Point out each leukocyte.
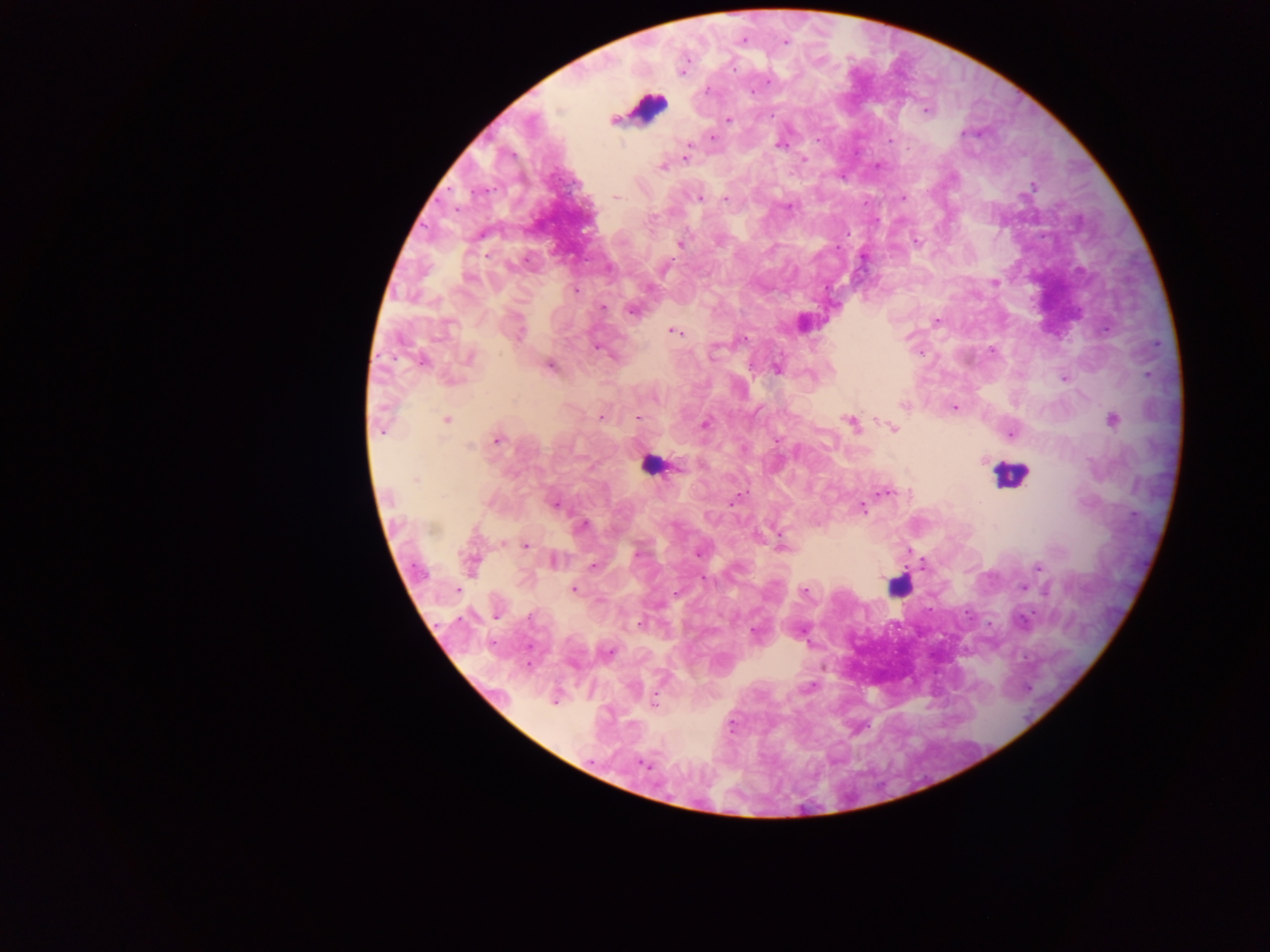
Approximate centers as [x, y] in pixels.
Leukocytes: [648, 108], [650, 465], [1008, 473], [899, 586].

Summary:
  - Malaria parasite locations: [744, 40], [786, 42], [733, 68], [683, 73], [768, 81], [707, 91], [750, 92], [926, 110], [613, 120], [729, 120], [965, 133], [712, 137], [817, 139], [890, 140], [688, 145], [780, 145], [686, 158], [803, 160], [662, 167], [1033, 185], [616, 197], [700, 198], [903, 198], [725, 199], [789, 206], [917, 241], [680, 244], [667, 266], [469, 278], [995, 282], [575, 291], [603, 308], [632, 311], [936, 322], [675, 332], [743, 339], [992, 350], [469, 358], [423, 362], [549, 366], [777, 368], [1064, 378], [655, 399], [903, 405], [954, 407], [601, 418], [637, 419], [1113, 419], [446, 420], [851, 422], [705, 425], [893, 428], [1011, 434], [497, 440], [777, 440], [469, 446], [415, 480], [886, 493], [554, 504], [862, 508], [584, 525], [525, 546], [782, 547], [638, 554], [697, 554], [553, 560], [471, 564], [594, 565], [1038, 566], [1022, 587], [457, 589], [573, 589], [805, 592], [677, 593], [495, 616], [1023, 620], [639, 624], [754, 632], [609, 652], [555, 702], [654, 703], [644, 764]
  - Image size: 1270×952 pixels
  - Capture: mobile-phone photograph through a microscope
  - Field of view: single
  - Preparation: thick blood film
  - Country: Ghana